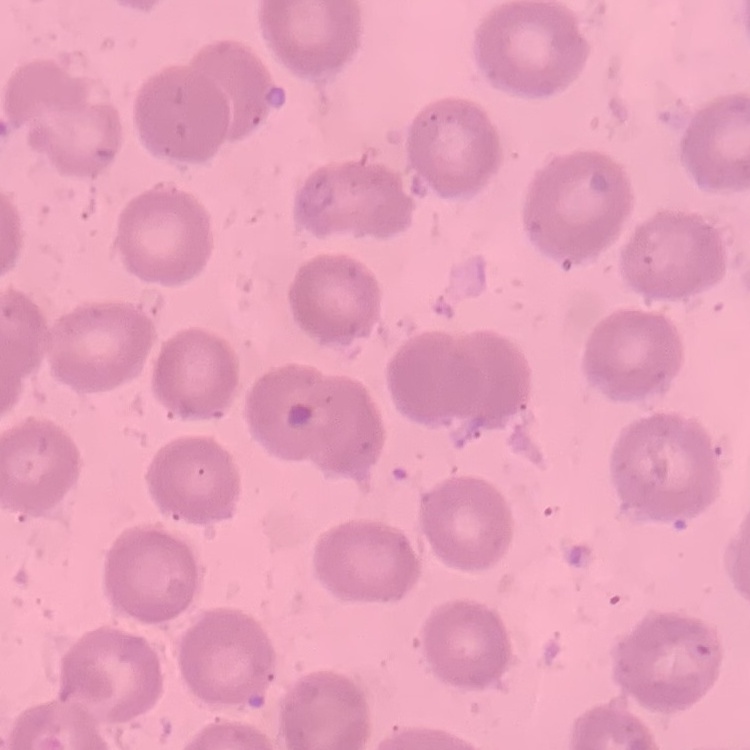
The erythrocytes show no rouleaux formation. Square crop of a larger photomicrograph. Field's or Giemsa stain. Thin blood film.